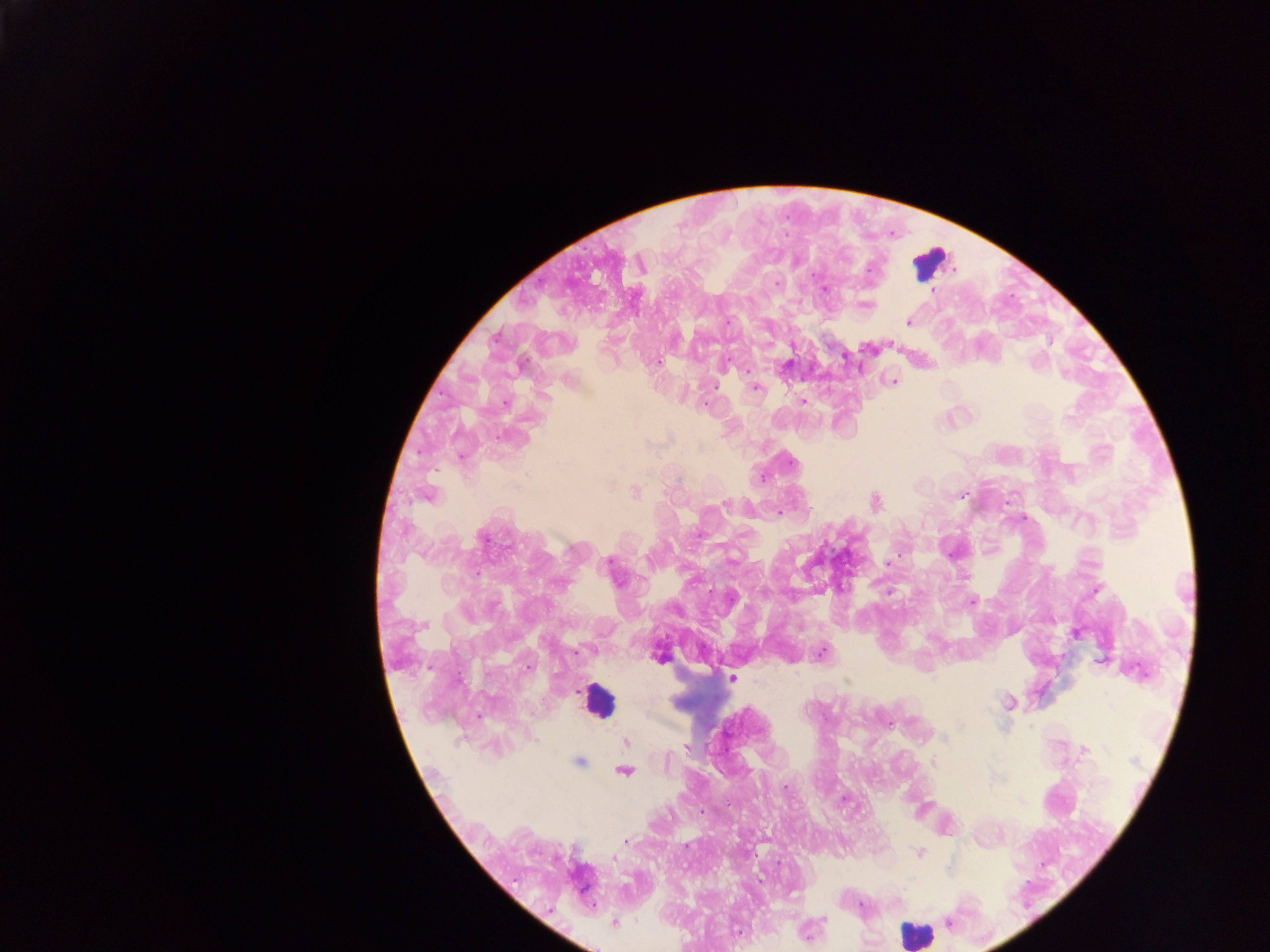
Approximate centers as x y in pixels.
Summary:
  - Leukocyte locations: 929 263; 931 275; 598 701; 916 933
  - Malaria parasite locations: 640 265; 777 283; 823 288; 932 290; 866 304; 908 322; 890 343; 845 356; 657 361; 785 366; 747 369; 568 380; 892 381; 755 387; 803 401; 505 402; 706 403; 461 456; 635 492; 962 493; 427 495; 875 502; 724 503; 779 512; 887 564; 611 567; 972 600; 1075 632; 822 652; 657 653; 1100 661; 731 678; 1009 702; 889 724; 625 742; 687 746; 1084 749; 578 761; 933 763; 623 770; 844 799; 624 840; 919 852; 614 923; 736 931; 807 932
  - Capture: mobile-phone photograph through a microscope
  - Field of view: single
  - Country: Ghana
  - Preparation: thick blood film
  - Image size: 1270×952 pixels